Assess the morphology of the erythrocytes.
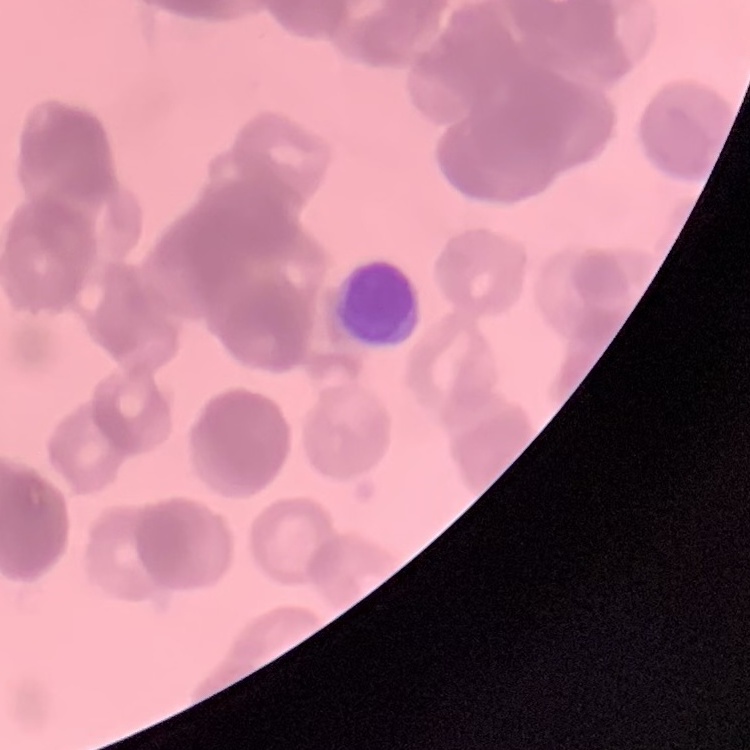

Rouleaux formation.

Summary:
  - Preparation: thin blood film
  - Image type: one tile cut from a larger photomicrograph
  - Stain: Field's or Giemsa